Assess the morphology of the erythrocytes.
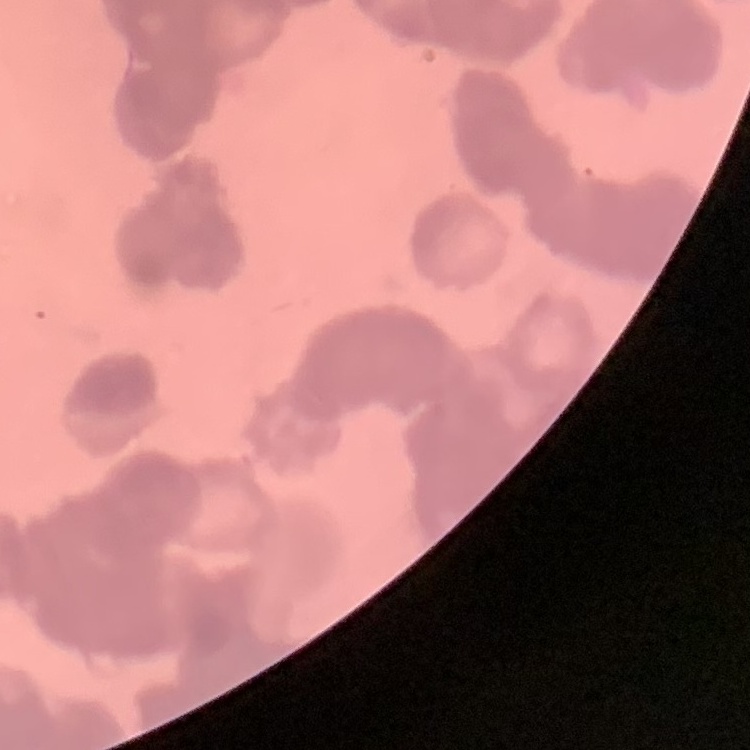
Rouleaux formation.

Field's or Giemsa stain. One tile cut from a larger photomicrograph. Thin peripheral smear.